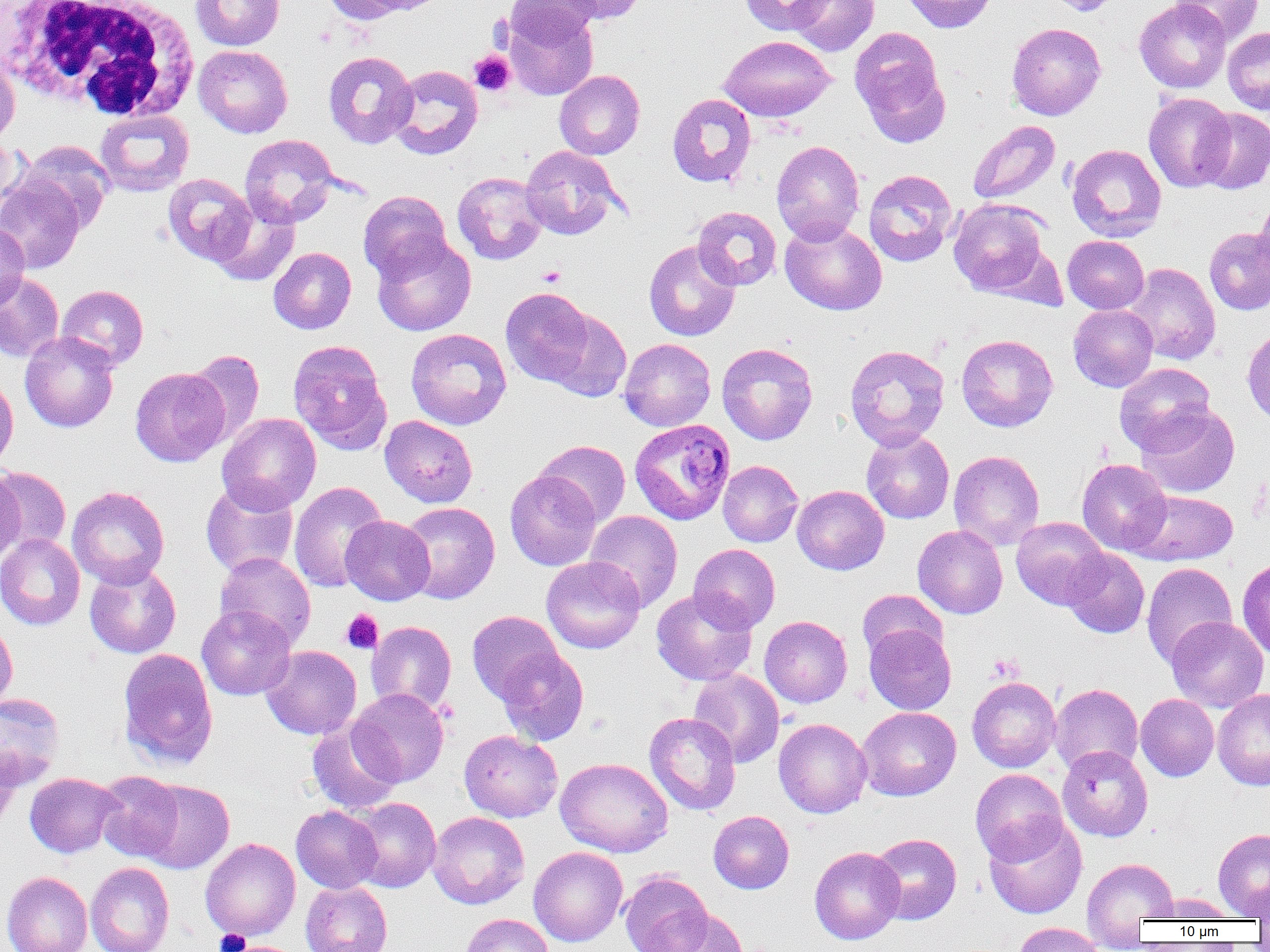
slide-level diagnosis = Plasmodium ovale
field of view = one of a larger specimen
platelet locations = approximate bounding boxes as (x1,y1)-(x2,y2) corner pairs in pixels: (469,50)-(515,96), (537,265)-(566,287), (341,609)-(383,654), (215,929)-(251,952)
image size = 1270×952 pixels
modality = light microscopy
magnification = 1000x
white blood cell locations = approximate bounding boxes as (x1,y1)-(x2,y2) corner pairs in pixels: (1,0)-(201,122)
uninfected red blood cell locations = approximate bounding boxes as (x1,y1)-(x2,y2) corner pairs in pixels: (190,0)-(285,51), (321,0)-(409,25), (361,0)-(449,15), (506,0)-(601,48), (552,0)-(649,24), (739,0)-(833,36), (788,0)-(879,56), (899,0)-(998,33), (1047,0)-(1121,16), (1134,0)-(1231,93), (1170,0)-(1262,45), (503,4)-(598,100), (1006,23)-(1106,120), (849,27)-(950,147), (1223,27)-(1270,115), (718,35)-(835,122), (194,45)-(293,138), (0,51)-(20,146), (323,51)-(417,149), (387,65)-(483,159), (554,70)-(645,160), (667,93)-(756,188), (1143,93)-(1236,192), (1196,107)-(1270,194), (95,109)-(194,197), (968,120)-(1060,204), (240,134)-(340,228), (0,136)-(23,222), (19,140)-(115,233), (771,140)-(865,245), (1067,144)-(1166,242), (520,146)-(623,239), (863,169)-(958,267), (452,171)-(548,265), (162,173)-(256,265), (0,174)-(86,274), (358,190)-(452,281), (210,196)-(300,287), (948,199)-(1052,297), (1252,200)-(1270,292), (692,206)-(782,290), (780,219)-(887,316), (0,222)-(30,310), (1204,227)-(1270,314), (371,234)-(476,336), (1062,236)-(1149,314), (643,240)-(741,341), (269,247)-(356,334), (1123,262)-(1221,365), (0,274)-(65,361), (56,285)-(149,371), (500,287)-(596,386), (1068,304)-(1158,392), (544,309)-(631,402), (406,328)-(511,429), (1242,329)-(1270,426), (19,331)-(119,433), (956,334)-(1058,432), (619,338)-(716,431), (287,340)-(392,454), (717,343)-(818,445), (844,344)-(950,450), (187,350)-(264,446), (1115,362)-(1216,454), (130,367)-(230,467), (0,373)-(18,471), (1136,404)-(1239,497), (216,413)-(321,515), (379,415)-(478,507), (861,430)-(954,524), (535,440)-(631,526), (949,450)-(1044,550), (1077,458)-(1172,556), (718,460)-(803,547), (0,466)-(71,553), (0,467)-(25,564), (505,470)-(601,570), (200,481)-(299,578), (289,481)-(388,593), (792,485)-(889,575), (67,486)-(169,588), (1129,489)-(1238,566), (398,502)-(500,604), (585,510)-(683,612), (341,515)-(435,605), (1011,516)-(1110,609), (913,524)-(1008,619), (0,533)-(85,630), (688,543)-(780,632), (1061,548)-(1149,638), (214,551)-(316,650), (541,556)-(645,654), (1237,557)-(1270,660), (84,563)-(182,658), (1141,563)-(1237,667), (651,589)-(757,686), (857,589)-(947,662), (196,606)-(297,700), (467,610)-(563,703), (760,616)-(852,708), (1166,616)-(1268,712), (0,619)-(18,711), (366,621)-(457,715), (864,623)-(956,715), (261,645)-(362,739), (118,648)-(218,771), (496,648)-(589,745), (688,668)-(784,768), (967,676)-(1061,772), (1050,683)-(1143,774), (1213,688)-(1270,790), (348,689)-(449,787), (0,693)-(64,789), (1136,694)-(1219,781), (857,707)-(961,801), (644,712)-(741,815), (774,718)-(872,818), (306,720)-(403,815), (459,730)-(562,822), (1057,745)-(1153,841), (0,746)-(21,834), (556,757)-(672,857), (970,769)-(1068,865), (93,770)-(185,862), (25,772)-(122,858), (138,779)-(234,873), (347,797)-(441,892), (291,805)-(383,893), (708,810)-(794,894), (427,811)-(530,909), (984,818)-(1087,918), (1213,828)-(1270,919), (869,833)-(961,924), (200,838)-(300,940), (529,846)-(628,947), (809,846)-(905,944), (1082,857)-(1179,932), (85,861)-(174,952), (2,871)-(92,952), (620,871)-(712,952), (300,881)-(392,952), (1249,884)-(1270,926), (1149,893)-(1237,921), (649,907)-(749,951), (460,914)-(553,952), (1011,922)-(1106,952)
preparation = thin blood film
Plasmodium ovale-infected red blood cell locations = approximate bounding boxes as (x1,y1)-(x2,y2) corner pairs in pixels: (630,418)-(735,525)